State which cell type is depicted.
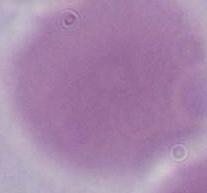

This is an erythrocyte.

Summary:
  - Modality: photomicrograph
  - Magnification: 1000x